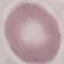

malaria_status: uninfected
preparation: thin blood film
capture: smartphone through the microscope eyepiece
image_type: cell patch, automatically extracted from a larger field of view and resized to 64 × 64 pixels
stain: Giemsa